Evaluate for parasitized red blood cells.
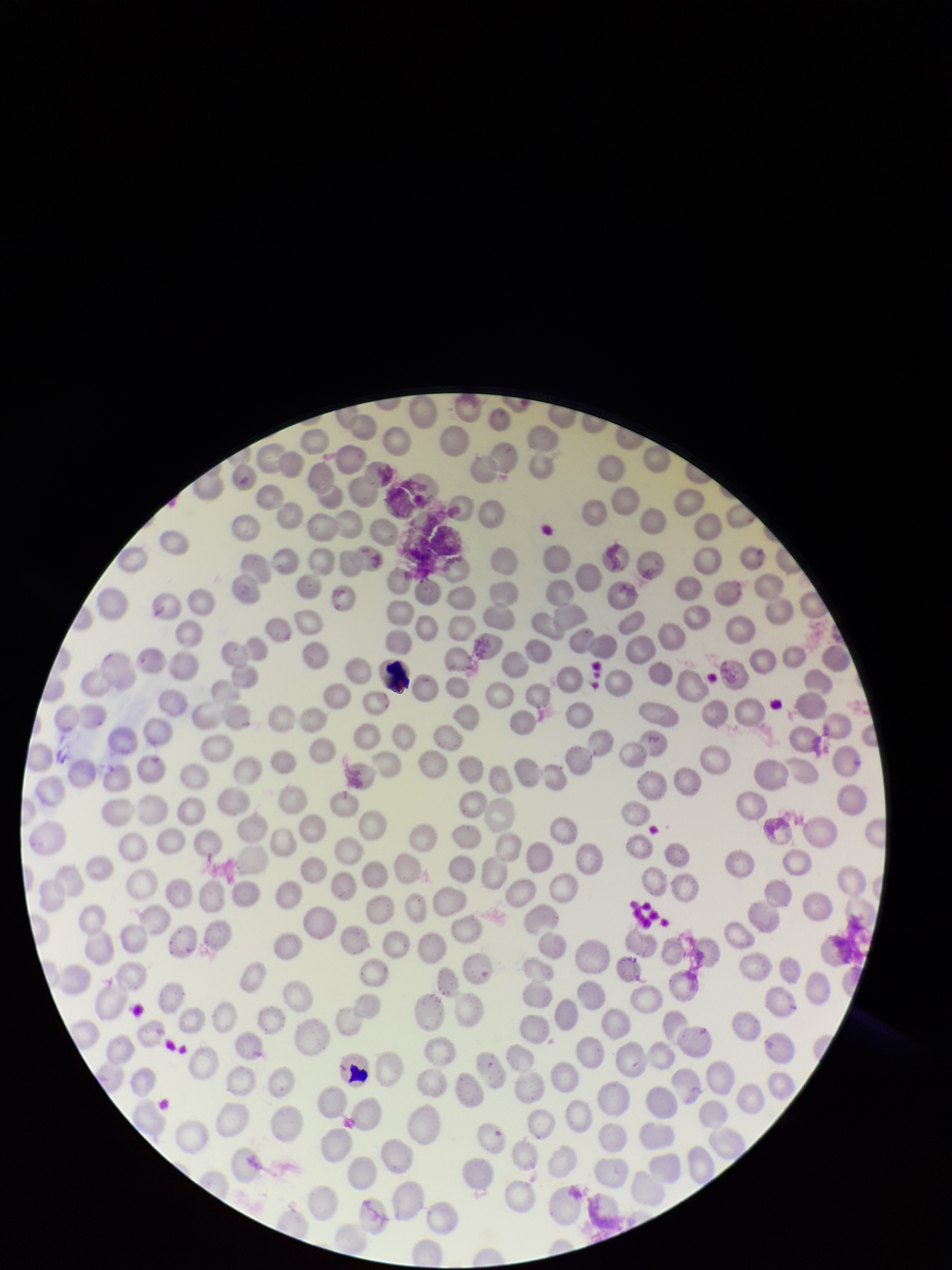
None seen.

Summary:
  - Image size: 952×1270 pixels
  - Stain: Giemsa
  - Preparation: thin blood smear
  - Patient malaria status: negative
  - Field of view: one from this slide
  - Red blood cell count: 243
  - Capture: smartphone photograph through the microscope eyepiece
  - Parasitized red blood cell count: 0